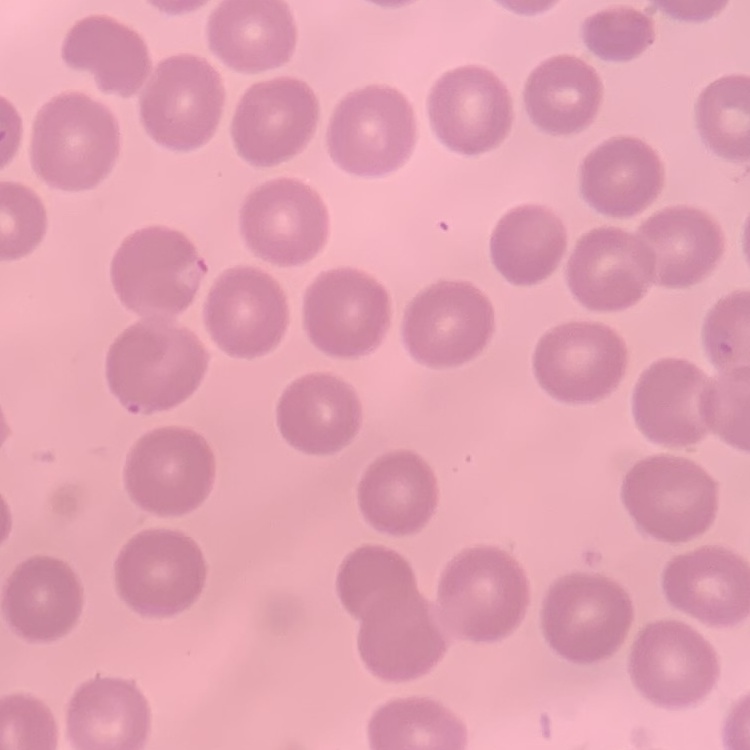
erythrocyte morphology = no rouleaux formation
image type = one tile cut from a larger photomicrograph
stain = Field's or Giemsa
preparation = thin blood smear